Locate every blood parasite and identify its species.
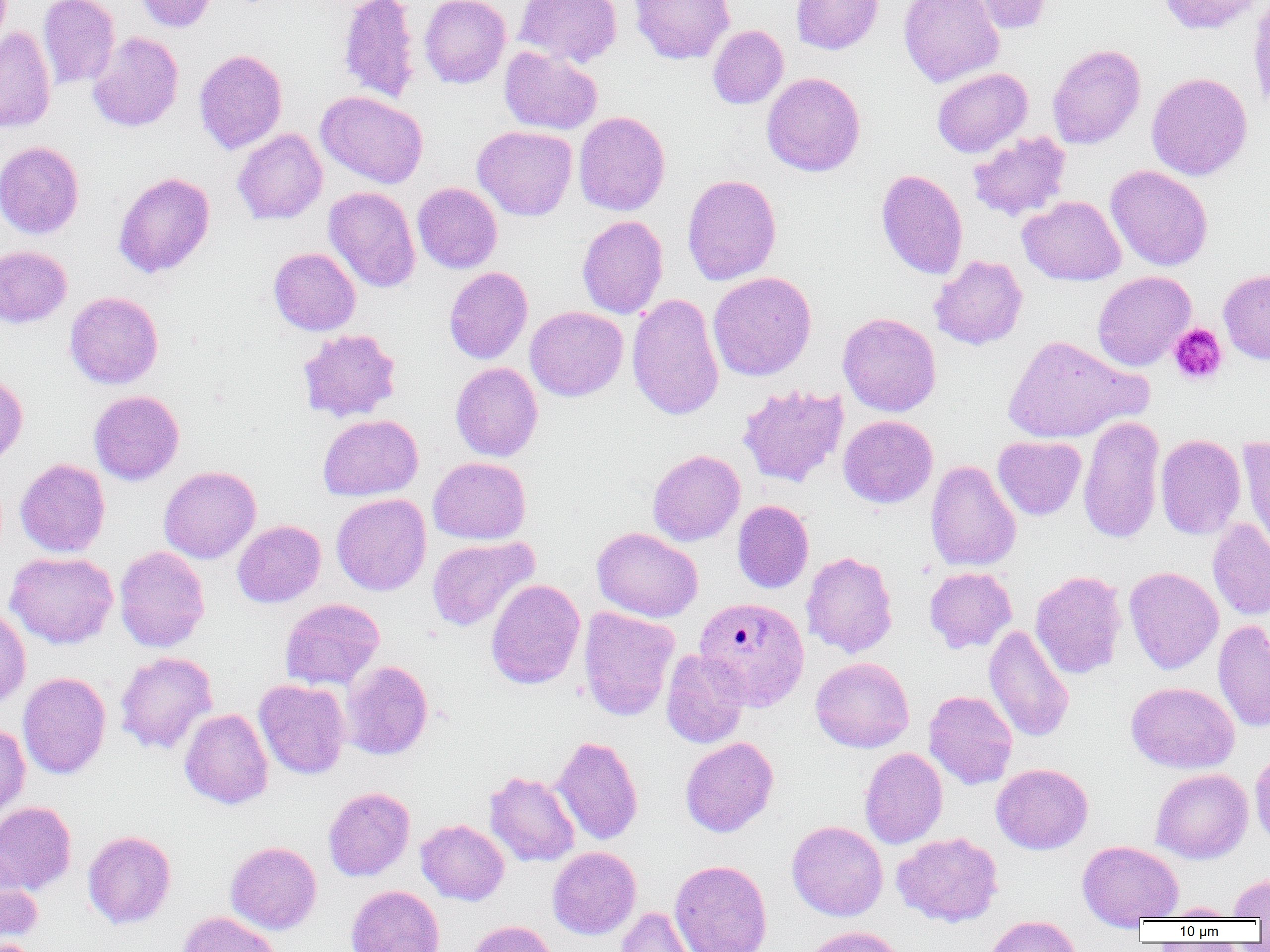

Approximate bounding boxes as (x1,y1)-(x2,y2) corner pairs in pixels.
Plasmodium vivax-infected red blood cells: (694,597)-(810,711).
No Plasmodium falciparum, Plasmodium ovale, Plasmodium malariae, Babesia divergens, or Trypanosoma brucei observed.

Summary:
  - Platelet locations: (1168,324)-(1228,386)
  - Uninfected red blood cell locations: (38,0)-(120,90), (135,0)-(217,32), (338,0)-(421,104), (419,0)-(511,88), (515,0)-(622,67), (630,0)-(735,64), (791,0)-(883,55), (899,0)-(1003,87), (965,0)-(1055,35), (1157,0)-(1266,35), (1248,0)-(1270,113), (708,25)-(789,109), (0,26)-(56,133), (87,32)-(184,132), (1047,44)-(1146,149), (499,46)-(602,135), (194,49)-(287,154), (932,67)-(1032,157), (762,72)-(865,177), (1146,72)-(1252,181), (316,90)-(428,189), (573,111)-(671,216), (473,125)-(577,221), (233,129)-(327,225), (967,132)-(1071,221), (0,141)-(85,239), (1106,165)-(1213,271), (876,168)-(968,279), (114,171)-(215,279), (682,173)-(782,286), (412,182)-(502,273), (323,187)-(421,292), (1018,196)-(1126,285), (577,215)-(668,319), (0,246)-(72,328), (268,247)-(361,335), (929,255)-(1028,350), (443,267)-(533,364), (1219,269)-(1270,364), (708,271)-(817,381), (1092,271)-(1196,371), (65,291)-(164,389), (626,293)-(724,421), (525,306)-(628,401), (837,312)-(941,416), (297,328)-(401,422), (1003,334)-(1147,444), (450,362)-(543,461), (0,372)-(28,467), (737,384)-(849,488), (89,390)-(184,485), (318,414)-(423,501), (838,415)-(938,508), (1077,416)-(1165,544), (1155,434)-(1246,539), (993,436)-(1086,520), (1238,436)-(1270,556), (647,449)-(745,546), (428,456)-(531,544), (15,458)-(110,557), (925,460)-(1021,572), (159,465)-(261,564), (331,493)-(431,596), (732,500)-(814,593), (1207,517)-(1270,620), (232,520)-(326,608), (592,527)-(703,622), (427,536)-(538,631), (114,546)-(210,652), (801,551)-(898,658), (5,552)-(118,648), (1124,566)-(1223,674), (924,567)-(1017,652), (1030,570)-(1127,679), (485,578)-(585,689), (280,598)-(385,691), (0,606)-(31,707), (578,606)-(680,722), (1213,619)-(1270,733), (984,623)-(1074,743), (661,650)-(750,748), (115,651)-(218,755), (671,652)-(761,835), (810,657)-(914,752), (340,660)-(433,760), (17,672)-(111,779), (253,679)-(351,779), (1127,681)-(1239,773), (924,690)-(1018,790), (179,708)-(273,809), (0,723)-(30,825), (552,735)-(643,845), (680,737)-(779,837), (860,747)-(948,849), (1250,747)-(1270,848), (991,763)-(1093,854), (1150,768)-(1253,863), (485,771)-(580,866), (323,786)-(415,881), (0,801)-(77,895), (416,819)-(510,905), (787,821)-(888,921), (83,830)-(176,929), (892,832)-(1004,927), (1077,840)-(1183,925), (226,841)-(322,934), (547,846)-(641,939), (669,859)-(772,952), (0,861)-(43,948), (1228,872)-(1270,919), (345,885)-(444,952), (1156,902)-(1240,920), (616,906)-(702,952), (177,912)-(283,952), (983,915)-(1082,952), (466,920)-(558,952), (801,926)-(906,952), (0,939)-(42,952)
  - Slide-level diagnosis: Plasmodium vivax
  - Field of view: one of a larger specimen
  - Preparation: thin blood smear
  - Magnification: 1000x
  - Modality: light microscopy
  - Image size: 1270×952 pixels